Locate every blood parasite and identify its species.
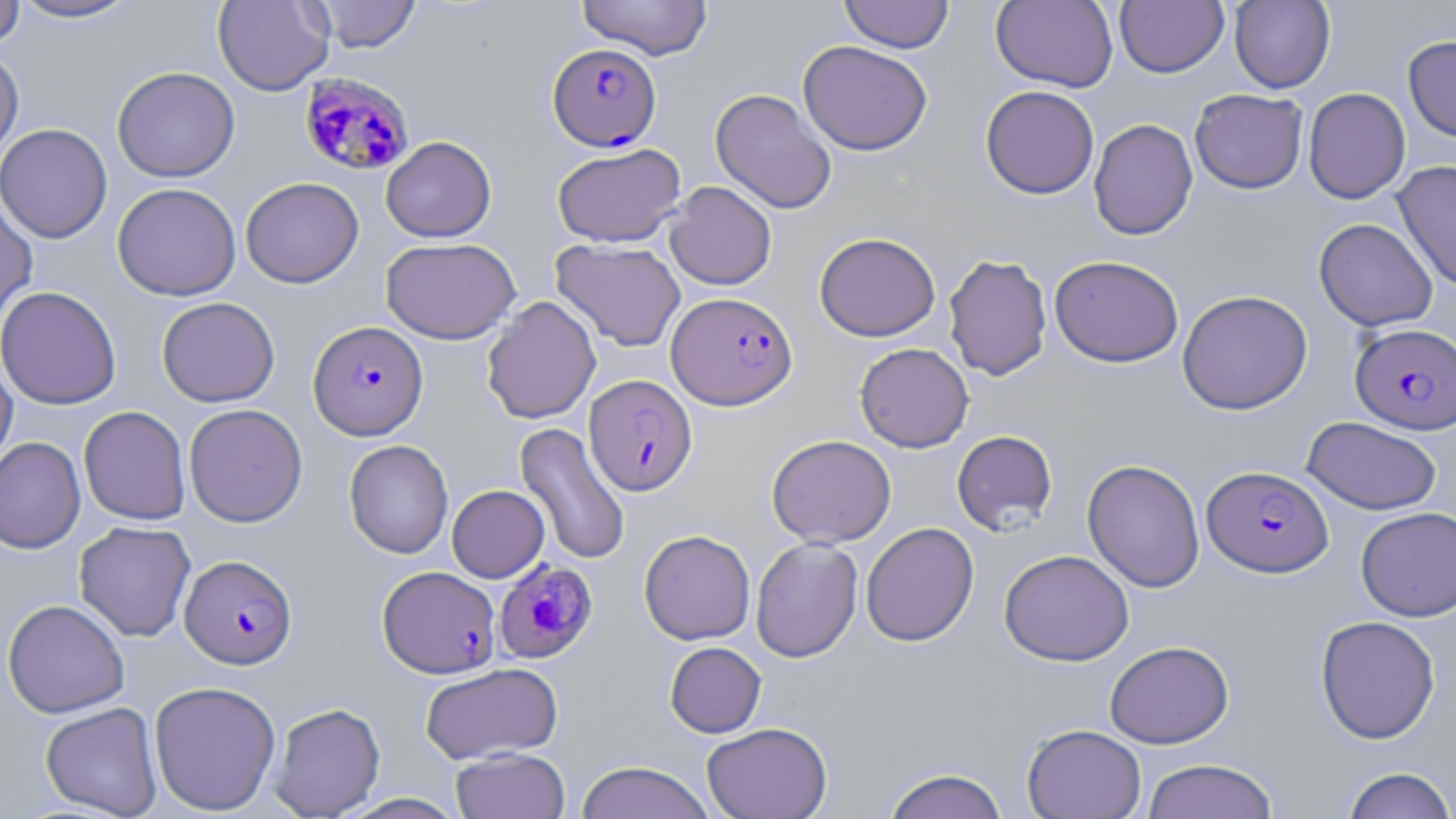

Approximate bounding boxes as [x1, y1, x2, y2] in pixels.
Plasmodium falciparum-infected red blood cells: [547, 42, 661, 151], [299, 72, 414, 176], [667, 291, 798, 410], [308, 321, 428, 440], [1350, 323, 1456, 434], [584, 374, 697, 496], [1202, 465, 1333, 577], [180, 554, 298, 669], [494, 560, 599, 663], [378, 565, 500, 678].
No Plasmodium ovale, Plasmodium malariae, Plasmodium vivax, Babesia divergens, or Trypanosoma brucei observed.

Summary:
  - Uninfected red blood cell locations: [9, 0, 142, 23], [213, 0, 334, 96], [312, 0, 421, 52], [576, 0, 713, 60], [838, 0, 955, 53], [990, 0, 1118, 93], [1115, 0, 1228, 78], [0, 1, 25, 49], [1229, 1, 1335, 93], [1403, 35, 1456, 142], [798, 40, 932, 155], [0, 47, 24, 163], [112, 66, 240, 182], [980, 85, 1099, 199], [1303, 87, 1410, 204], [710, 88, 837, 214], [1190, 89, 1308, 194], [1088, 119, 1197, 241], [0, 123, 112, 243], [381, 135, 496, 242], [552, 143, 686, 247], [1392, 160, 1456, 292], [240, 176, 364, 288], [664, 181, 777, 290], [112, 182, 241, 301], [0, 192, 38, 328], [1313, 218, 1438, 332], [814, 232, 941, 341], [381, 237, 521, 344], [551, 239, 686, 352], [943, 254, 1053, 381], [1049, 255, 1184, 368], [0, 286, 122, 410], [1177, 289, 1313, 414], [156, 296, 280, 407], [481, 296, 601, 424], [854, 342, 974, 452], [0, 353, 18, 470], [184, 403, 308, 527], [78, 406, 191, 525], [1302, 416, 1442, 515], [514, 422, 631, 566], [951, 430, 1058, 535], [767, 434, 896, 547], [0, 436, 86, 554], [344, 440, 453, 558], [1081, 459, 1205, 593], [447, 484, 549, 582], [1356, 506, 1456, 621], [74, 521, 196, 641], [861, 522, 979, 646], [639, 529, 755, 645], [750, 538, 863, 662], [999, 549, 1134, 666], [2, 599, 130, 718], [1315, 615, 1441, 743], [1104, 640, 1234, 748], [664, 641, 766, 738], [420, 662, 562, 764], [148, 680, 281, 815], [40, 702, 163, 818], [268, 702, 385, 818], [701, 721, 832, 819], [1021, 723, 1146, 819], [451, 747, 570, 819], [1141, 758, 1279, 819], [575, 760, 715, 819], [1340, 766, 1456, 818], [880, 767, 1010, 818], [339, 793, 468, 818]
  - Slide-level diagnosis: Plasmodium falciparum
  - Preparation: thin blood film
  - Stain: May-Grünwald-Giemsa
  - Modality: optical microscopy
  - Magnification: 1000x
  - Field of view: one of a larger specimen
  - Image size: 1456×819 pixels